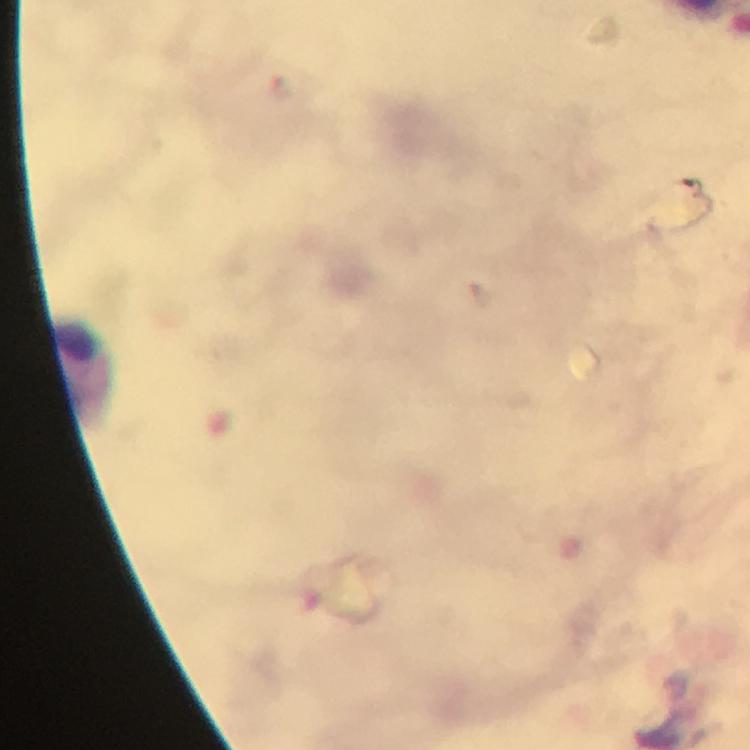

magnification = 100x
malaria parasites = none seen
cropped from = a single field of view
preparation = thick blood film
leukocyte locations = approximate centers as [x, y] in pixels: [87, 372]
capture = smartphone photograph through a microscope
context = from a diagnostic examination for malaria
image size = 750×750 pixels
immersion oil = used
stain = Giemsa